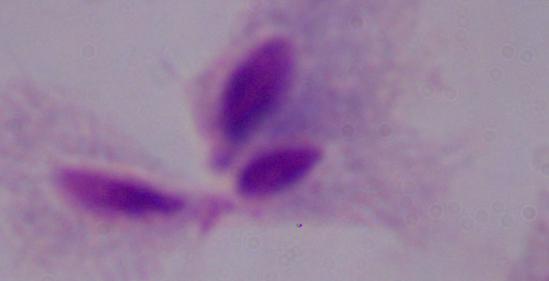
modality = micrograph
identification = trichomonad
magnification = 1000x